Classify this cell by malaria status.
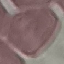
Uninfected.

Summary:
  - Preparation: thin smear
  - Image type: automatically extracted cell patch, resized to 64 × 64 pixels
  - Stain: Giemsa
  - Capture: smartphone through the microscope eyepiece